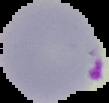

result: malaria parasites identified
image_type: segmented cell region on a black background
image_size: 109×103 pixels
preparation: thin blood film